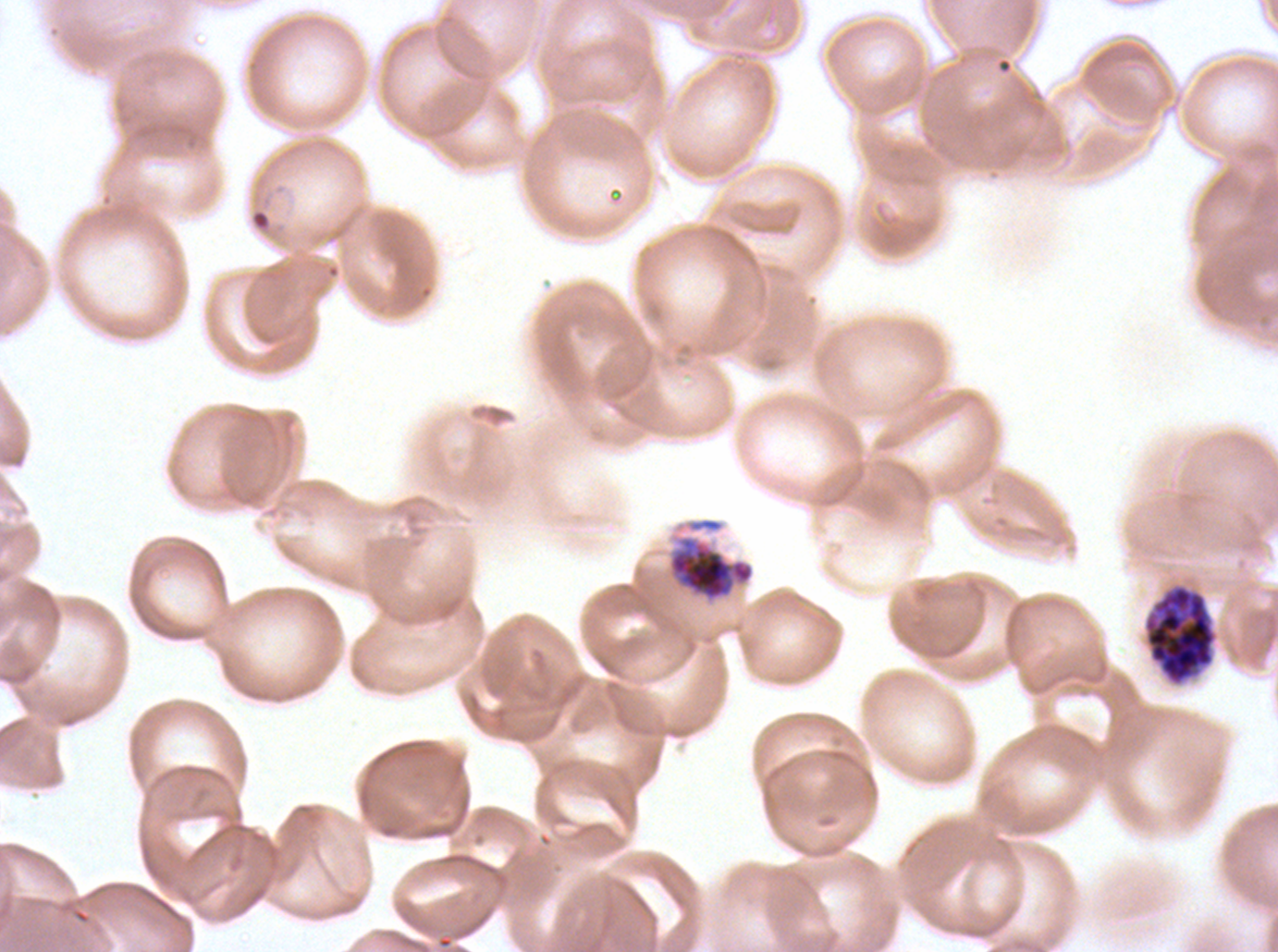

notation = approximate bounding boxes as [x1, y1, x2, y2] in pixels
early schizont locations = [668, 535, 755, 602]
late schizont locations = [1144, 585, 1216, 685]
field of view = sub-image separated from a larger composite
image size = 1278×952 pixels
specimen = P. falciparum cultured ex vivo for 24 to 48 hours, from a patient in The Gambia
stain = Giemsa
preparation = thin blood smear
life-cycle stages observed = early schizont, late schizont